Locate and identify every blood parasite.
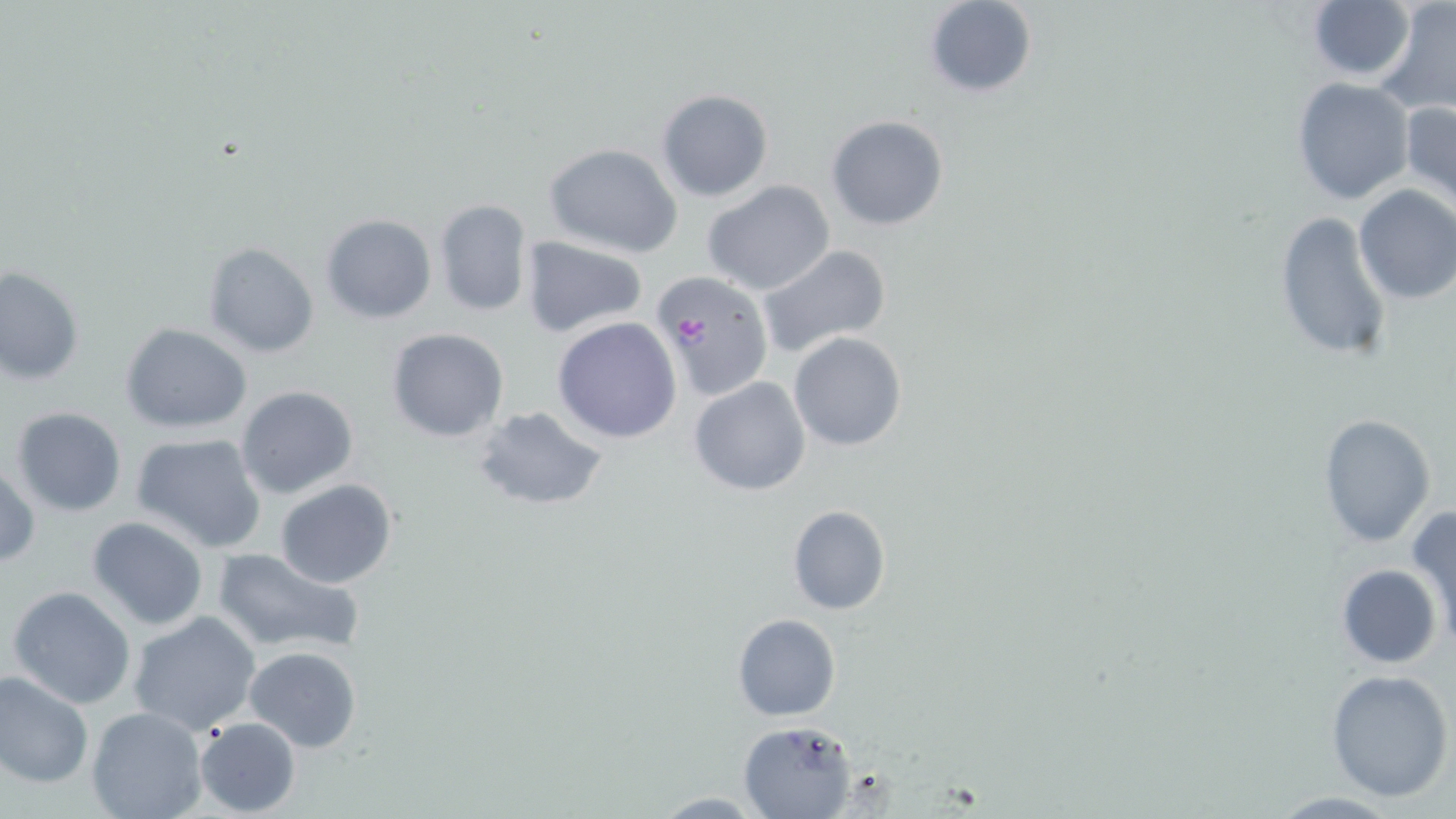
Approximate bounding boxes as (x1, y1, x2, y2) in pixels.
Plasmodium falciparum-infected red blood cells: (649, 269, 775, 402).
No Plasmodium ovale, Plasmodium malariae, Plasmodium vivax, Babesia divergens, or Trypanosoma brucei observed.

Uninfected red blood cell locations: (923, 0, 1038, 98), (1375, 1, 1456, 117), (1303, 2, 1417, 82), (1291, 78, 1415, 205), (655, 89, 775, 203), (1401, 101, 1456, 213), (826, 116, 949, 230), (543, 143, 683, 258), (702, 180, 837, 296), (1353, 184, 1456, 306), (434, 198, 533, 317), (1274, 210, 1397, 367), (319, 213, 437, 324), (520, 236, 649, 339), (204, 242, 320, 358), (756, 244, 892, 358), (2, 266, 85, 386), (551, 316, 682, 443), (121, 323, 253, 433), (385, 326, 510, 442), (787, 331, 908, 453), (688, 375, 813, 496), (235, 384, 360, 500), (471, 404, 610, 513), (9, 407, 127, 516), (1317, 413, 1436, 547), (130, 431, 268, 552), (1, 462, 40, 569), (275, 479, 399, 588), (786, 504, 891, 615), (1407, 505, 1456, 645), (85, 516, 208, 631), (212, 546, 365, 656), (1336, 563, 1442, 669), (6, 585, 137, 709), (127, 610, 262, 735), (731, 613, 841, 721), (243, 646, 362, 751), (0, 669, 94, 790), (1325, 669, 1454, 801), (85, 707, 208, 819), (193, 716, 301, 817), (738, 720, 858, 818), (648, 793, 772, 817). Slide-level diagnosis: Plasmodium falciparum. Optical microscopy. Captured at 1000x magnification. Thin blood smear. One field of a larger specimen. May-Grünwald-Giemsa stain. Image is 1456×819 pixels.